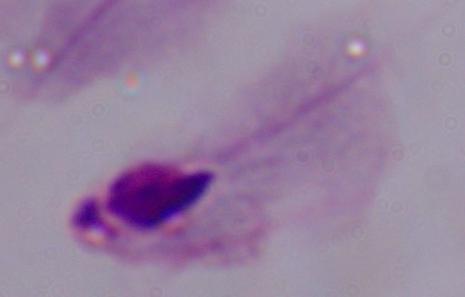

magnification: 1000x
modality: micrograph
identification: trichomonad